Assess this cell for malaria.
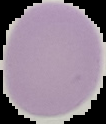
Uninfected.

image size = 106×124 pixels
preparation = thin blood film
image type = segmented cell region on a black background